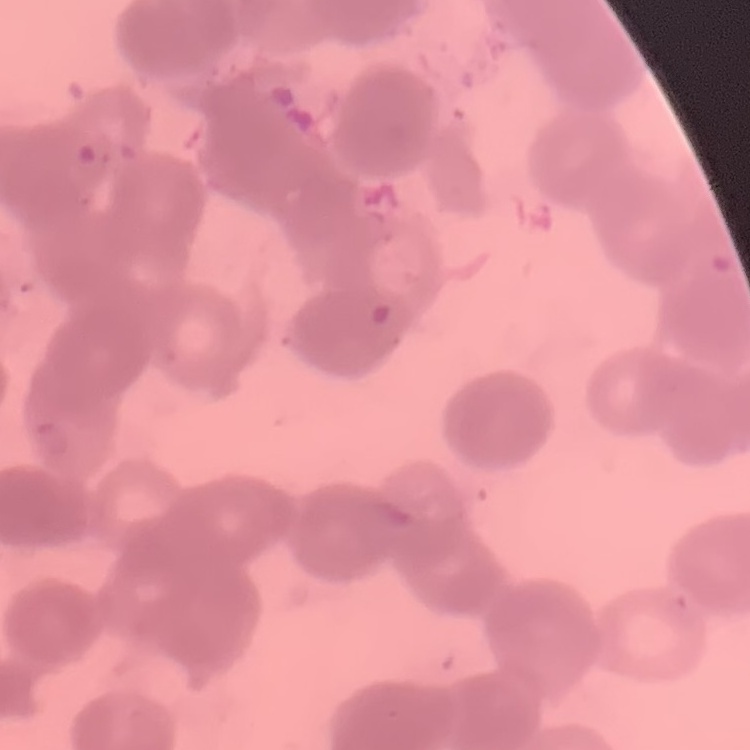

The red blood cells exhibit rouleaux formation. Square crop of a larger photomicrograph. Stained with either Field's or Giemsa. Thin blood film.